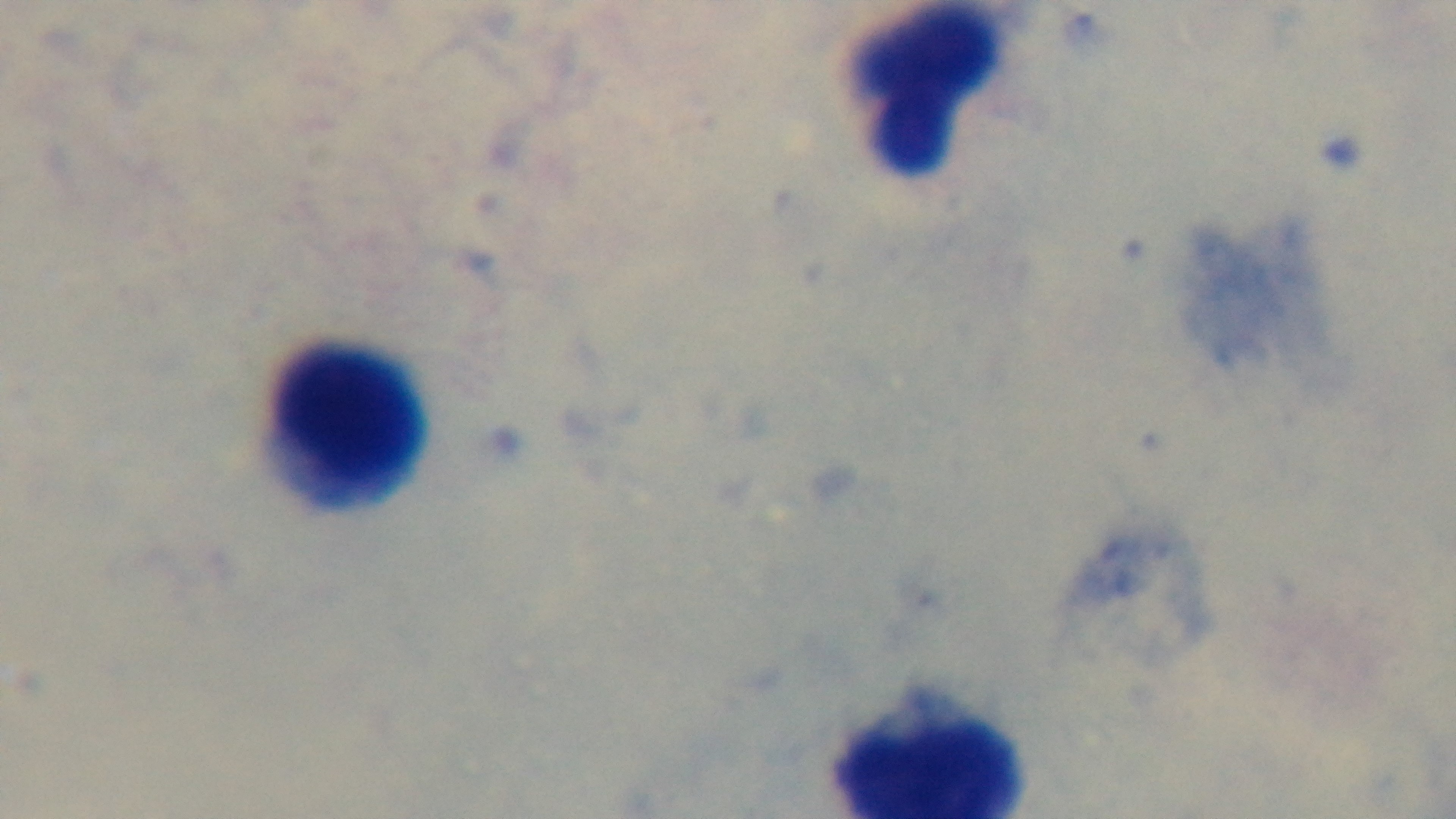 Captured with a mounted 4K digital camera. Preparation: thick smear. Malaria status: uninfected. Photomicrograph. Giemsa stain. Single field of view. Oil-immersion objective, 100x.